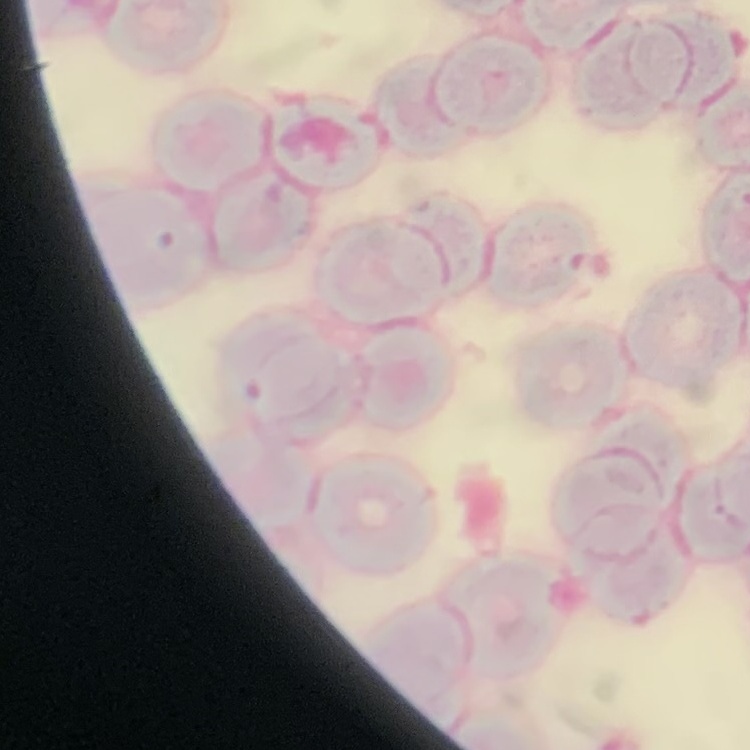
Summary:
  - Erythrocyte morphology: rouleaux formation
  - Preparation: thin peripheral smear
  - Stain: Field's or Giemsa
  - Image type: one tile cut from a larger photomicrograph